Classify this cell by malaria status.
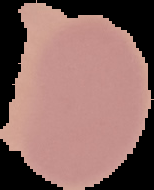

Uninfected.

image type = segmented cell region on a black background
image size = 154×190 pixels
preparation = thin blood film